Assess this cell for malaria.
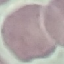

Uninfected.

Photographed with a smartphone camera at the microscope eyepiece. Automatically extracted cell patch, resized to 64 × 64 pixels. Thin smear of blood. Giemsa stain.